Locate every blood parasite and identify its species.
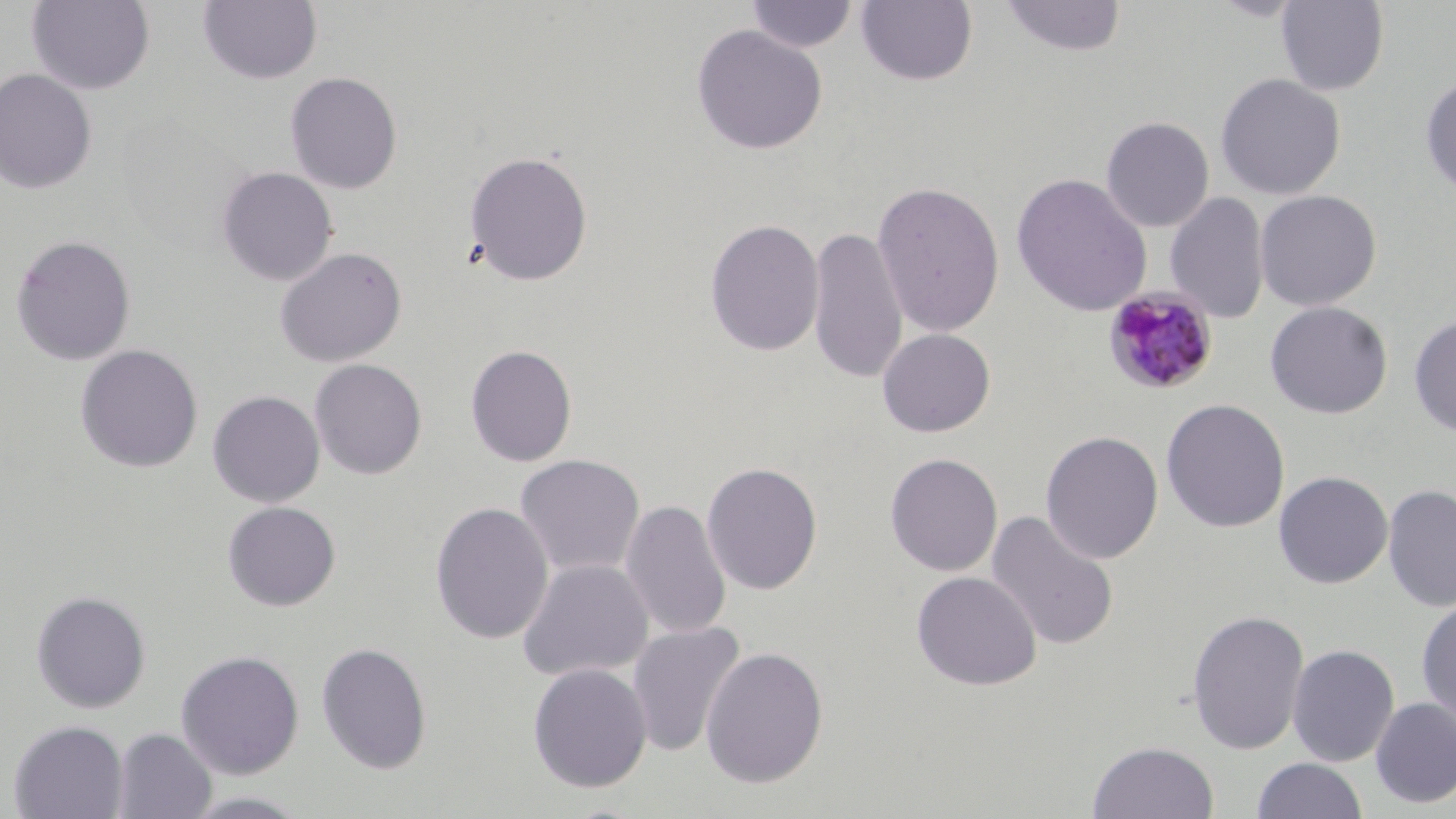

Approximate bounding boxes as named x1/y1/x2/y2 corners in pixels.
Plasmodium malariae-infected red blood cells: (x1=1101, y1=286, x2=1220, y2=397).
No Plasmodium falciparum, Plasmodium ovale, Plasmodium vivax, Babesia divergens, or Trypanosoma brucei observed.

Summary:
  - Uninfected red blood cell locations: (x1=999, y1=0, x2=1127, y2=58), (x1=26, y1=1, x2=155, y2=95), (x1=197, y1=1, x2=323, y2=85), (x1=745, y1=1, x2=860, y2=53), (x1=855, y1=1, x2=978, y2=87), (x1=1275, y1=1, x2=1389, y2=96), (x1=691, y1=24, x2=828, y2=155), (x1=0, y1=68, x2=97, y2=194), (x1=284, y1=71, x2=403, y2=194), (x1=1215, y1=73, x2=1345, y2=200), (x1=1420, y1=74, x2=1456, y2=198), (x1=1101, y1=116, x2=1215, y2=232), (x1=463, y1=150, x2=593, y2=286), (x1=217, y1=166, x2=338, y2=285), (x1=1011, y1=173, x2=1152, y2=316), (x1=871, y1=180, x2=1006, y2=337), (x1=1254, y1=190, x2=1382, y2=311), (x1=1165, y1=192, x2=1270, y2=324), (x1=704, y1=219, x2=825, y2=356), (x1=807, y1=226, x2=909, y2=384), (x1=10, y1=235, x2=135, y2=366), (x1=274, y1=247, x2=407, y2=368), (x1=1264, y1=301, x2=1393, y2=419), (x1=1408, y1=314, x2=1456, y2=436), (x1=877, y1=328, x2=995, y2=437), (x1=75, y1=344, x2=203, y2=473), (x1=465, y1=344, x2=578, y2=467), (x1=310, y1=359, x2=427, y2=479), (x1=207, y1=390, x2=325, y2=507), (x1=1161, y1=398, x2=1290, y2=533), (x1=1040, y1=430, x2=1164, y2=564), (x1=884, y1=452, x2=1003, y2=577), (x1=514, y1=454, x2=645, y2=578), (x1=701, y1=461, x2=823, y2=595), (x1=1274, y1=471, x2=1393, y2=589), (x1=1382, y1=484, x2=1456, y2=613), (x1=621, y1=499, x2=731, y2=640), (x1=222, y1=501, x2=341, y2=611), (x1=429, y1=501, x2=553, y2=644), (x1=985, y1=510, x2=1120, y2=652), (x1=517, y1=559, x2=654, y2=682), (x1=911, y1=571, x2=1042, y2=691), (x1=30, y1=590, x2=151, y2=713), (x1=1416, y1=598, x2=1456, y2=728), (x1=1187, y1=609, x2=1309, y2=755), (x1=626, y1=621, x2=746, y2=757), (x1=316, y1=642, x2=433, y2=774), (x1=1287, y1=644, x2=1400, y2=767), (x1=700, y1=646, x2=829, y2=788), (x1=175, y1=649, x2=304, y2=779), (x1=527, y1=663, x2=652, y2=793), (x1=1370, y1=697, x2=1456, y2=808), (x1=7, y1=720, x2=129, y2=819), (x1=112, y1=727, x2=217, y2=819), (x1=1088, y1=741, x2=1219, y2=819), (x1=1251, y1=757, x2=1367, y2=819)
  - Slide-level diagnosis: Plasmodium malariae
  - Field of view: single
  - Image size: 1456×819 pixels
  - Magnification: 1000x
  - Preparation: thin blood smear
  - Stain: May-Grünwald-Giemsa
  - Modality: light microscopy